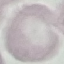 Malaria status: uninfected. Acquired by smartphone through the microscope eyepiece. Thin smear of blood. Automatically extracted cell patch, resized to 64 × 64 pixels. Giemsa-stained preparation.